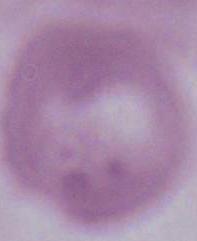
{
  "modality": "micrograph",
  "magnification": "1000x",
  "identification": "red blood cell"
}